Report the malaria status of this cell.
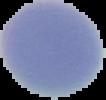

It is uninfected.

Segmented cell region on a black background. From a thin blood film. Image is 106×100 pixels.